Outline each Plasmodium ovale-infected red blood cell.
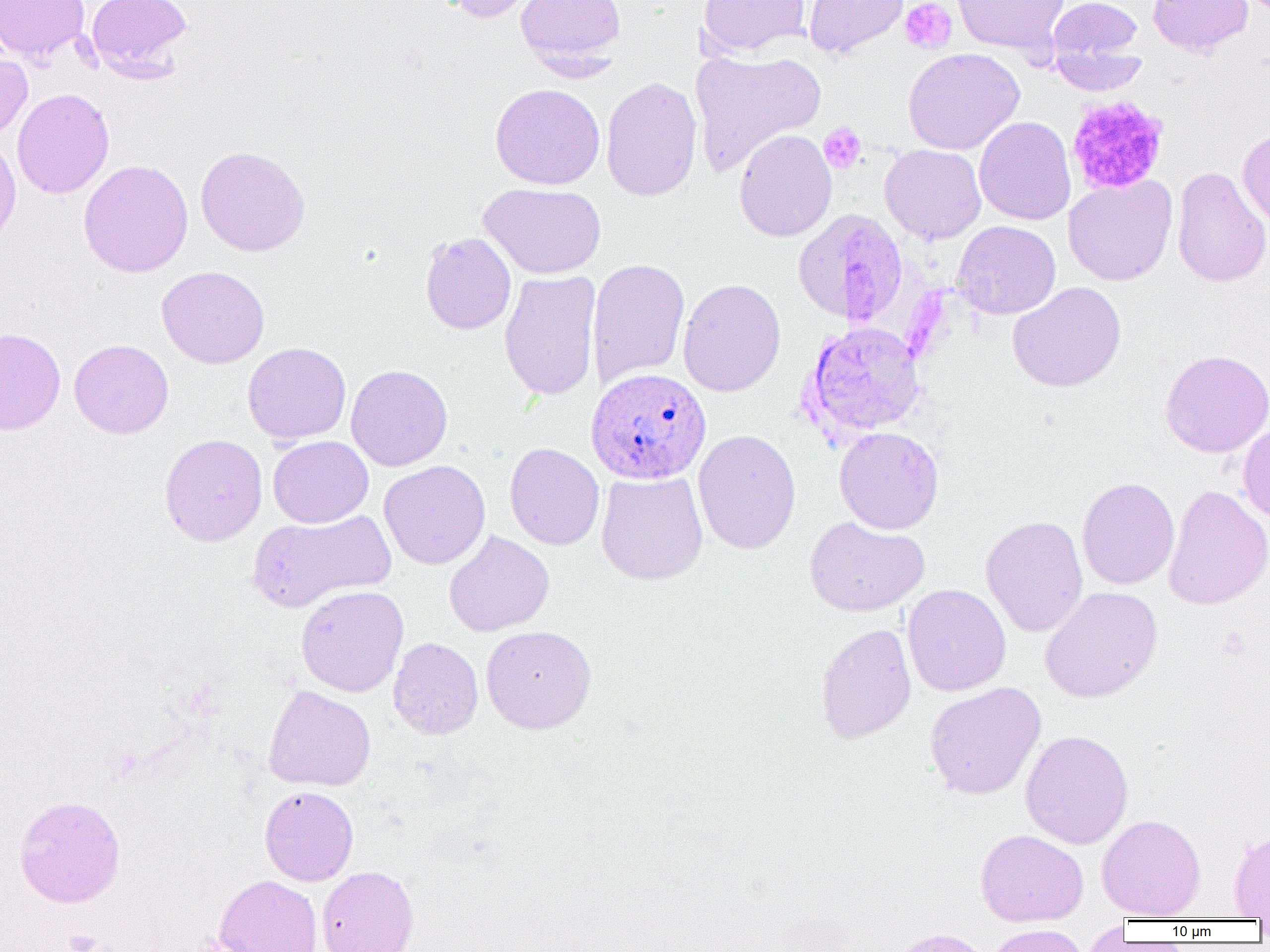
Approximate bounding boxes as [x1, y1, x2, y2] in pixels.
Plasmodium ovale-infected red blood cells: [586, 367, 711, 485].

Uninfected red blood cell locations: [0, 0, 90, 63], [86, 0, 193, 80], [441, 0, 548, 23], [515, 0, 625, 71], [697, 0, 811, 58], [803, 0, 908, 59], [953, 0, 1069, 57], [1046, 0, 1143, 72], [1147, 0, 1253, 58], [1050, 45, 1147, 96], [903, 48, 1024, 155], [689, 49, 826, 176], [0, 50, 32, 139], [601, 76, 702, 202], [489, 82, 605, 190], [12, 88, 115, 199], [974, 116, 1075, 225], [1237, 128, 1270, 227], [734, 129, 837, 242], [0, 134, 21, 252], [879, 144, 986, 244], [195, 145, 311, 256], [79, 159, 193, 278], [1171, 166, 1270, 288], [1062, 175, 1178, 286], [478, 182, 606, 279], [793, 207, 908, 326], [953, 220, 1061, 319], [420, 232, 516, 335], [587, 257, 690, 387], [157, 266, 269, 369], [498, 270, 601, 401], [677, 278, 786, 397], [1007, 281, 1126, 392], [801, 321, 927, 440], [0, 327, 66, 435], [69, 339, 174, 439], [242, 342, 352, 444], [1159, 349, 1270, 458], [346, 364, 453, 471], [1237, 422, 1270, 523], [834, 426, 944, 534], [692, 429, 802, 555], [159, 433, 268, 546], [267, 436, 374, 528], [504, 442, 604, 550], [379, 460, 491, 569], [596, 471, 708, 584], [1077, 476, 1179, 590], [1163, 484, 1270, 610], [248, 509, 396, 612], [980, 514, 1088, 637], [804, 515, 929, 617], [444, 529, 554, 637], [902, 584, 1011, 696], [296, 585, 409, 697], [1040, 585, 1162, 703], [815, 622, 916, 744], [480, 625, 597, 734], [388, 637, 483, 739], [924, 682, 1046, 800], [263, 685, 376, 791], [1020, 730, 1134, 849], [259, 785, 359, 885], [13, 794, 126, 908], [1096, 813, 1206, 920], [975, 828, 1088, 926], [1227, 830, 1270, 919], [317, 865, 419, 952], [214, 875, 323, 952], [1081, 920, 1130, 951], [984, 925, 1091, 952], [886, 928, 990, 952]. Platelet locations: [900, 0, 956, 54], [1066, 95, 1169, 196], [818, 122, 867, 174], [62, 929, 104, 952]. Slide-level diagnosis: Plasmodium ovale. 1000x magnification. One field of a larger specimen. Image is 1270×952 pixels. Thin blood smear. Optical microscopy.